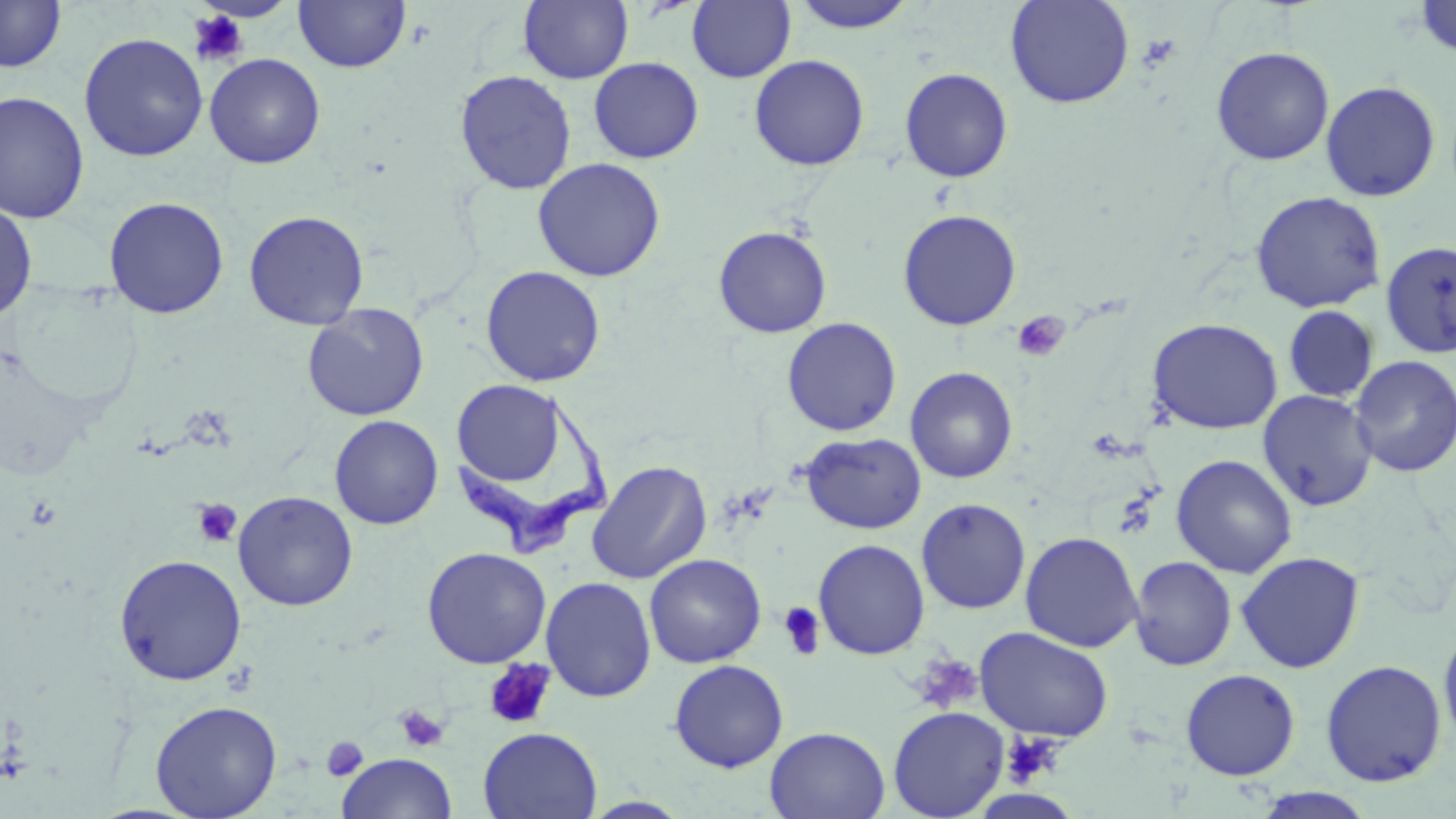
Summary:
  - Coordinate format: approximate bounding boxes as (x1,y1)-(x2,y2) corner pairs in pixels
  - Uninfected red blood cell locations: (294,0)-(410,73), (1005,0)-(1135,109), (1414,0)-(1456,59), (0,1)-(67,73), (519,1)-(633,84), (686,1)-(796,84), (789,1)-(919,33), (78,33)-(208,162), (1211,45)-(1334,165), (204,53)-(325,169), (750,54)-(869,171), (589,57)-(704,163), (899,67)-(1013,183), (454,70)-(577,195), (1320,80)-(1441,202), (0,91)-(90,224), (532,157)-(666,282), (1250,191)-(1386,314), (103,196)-(229,319), (0,201)-(38,321), (897,209)-(1022,330), (243,210)-(369,330), (713,225)-(832,338), (1379,240)-(1456,359), (480,265)-(606,387), (302,303)-(430,421), (1283,305)-(1380,402), (782,317)-(902,436), (1147,317)-(1283,434), (1349,355)-(1456,477), (905,367)-(1018,484), (451,379)-(567,487), (1258,390)-(1378,511), (329,415)-(443,529), (800,432)-(926,534), (1171,454)-(1298,578), (586,460)-(712,584), (233,491)-(358,611), (916,498)-(1031,614), (1020,531)-(1144,652), (813,539)-(930,659), (421,547)-(552,668), (1235,551)-(1365,673), (113,553)-(248,686), (645,553)-(766,667), (1129,556)-(1237,671), (540,576)-(657,703), (1438,623)-(1456,752), (976,627)-(1114,742), (669,659)-(789,772), (1320,659)-(1447,787), (1180,668)-(1301,781), (150,700)-(282,818), (888,706)-(1010,818), (478,726)-(602,819), (765,726)-(890,818), (337,753)-(456,819), (1251,787)-(1377,819)
  - Platelet locations: (187,10)-(249,67), (1138,34)-(1181,71), (1012,311)-(1070,363), (192,498)-(243,548), (778,601)-(826,661), (911,653)-(983,714), (483,658)-(556,729), (393,704)-(450,753), (1001,732)-(1065,787), (322,736)-(368,781)
  - Trypanosoma brucei locations: (450,392)-(612,556)
  - Slide-level diagnosis: Trypanosoma brucei
  - Image size: 1456×819 pixels
  - Field of view: single
  - Magnification: 1000x
  - Stain: May-Grünwald-Giemsa
  - Preparation: thin blood smear
  - Modality: light microscopy